Assess this cell for malaria.
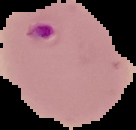
It is parasitized.

Summary:
  - Preparation: thin blood film
  - Image type: cell region segmented out of the field of view; surrounding area masked to black
  - Image size: 136×130 pixels